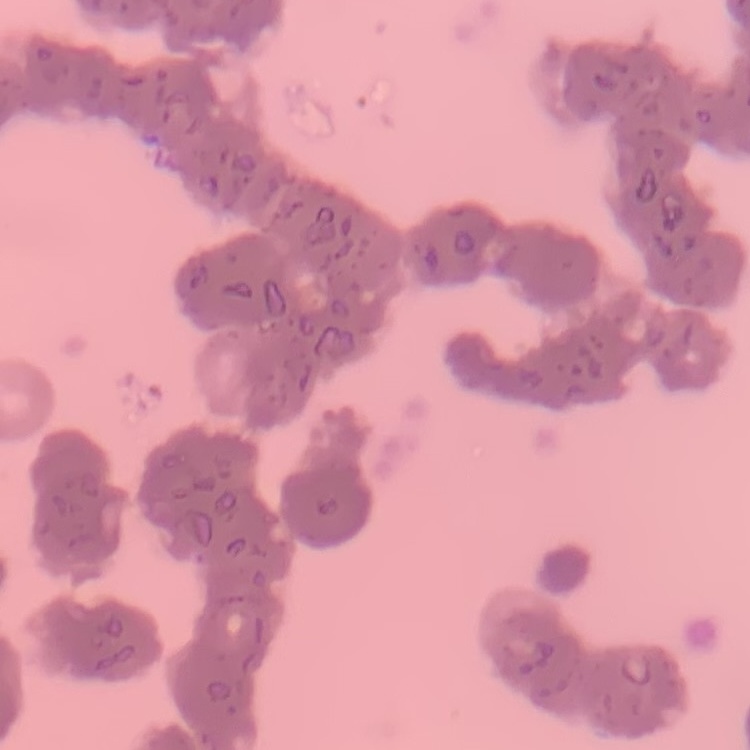

The erythrocytes show rouleaux formation. Field's or Giemsa stain. Square crop of a larger photomicrograph. Thin blood film.